Identify the cell.
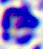
A leukocyte.

Micrograph. Captured at 400x magnification.